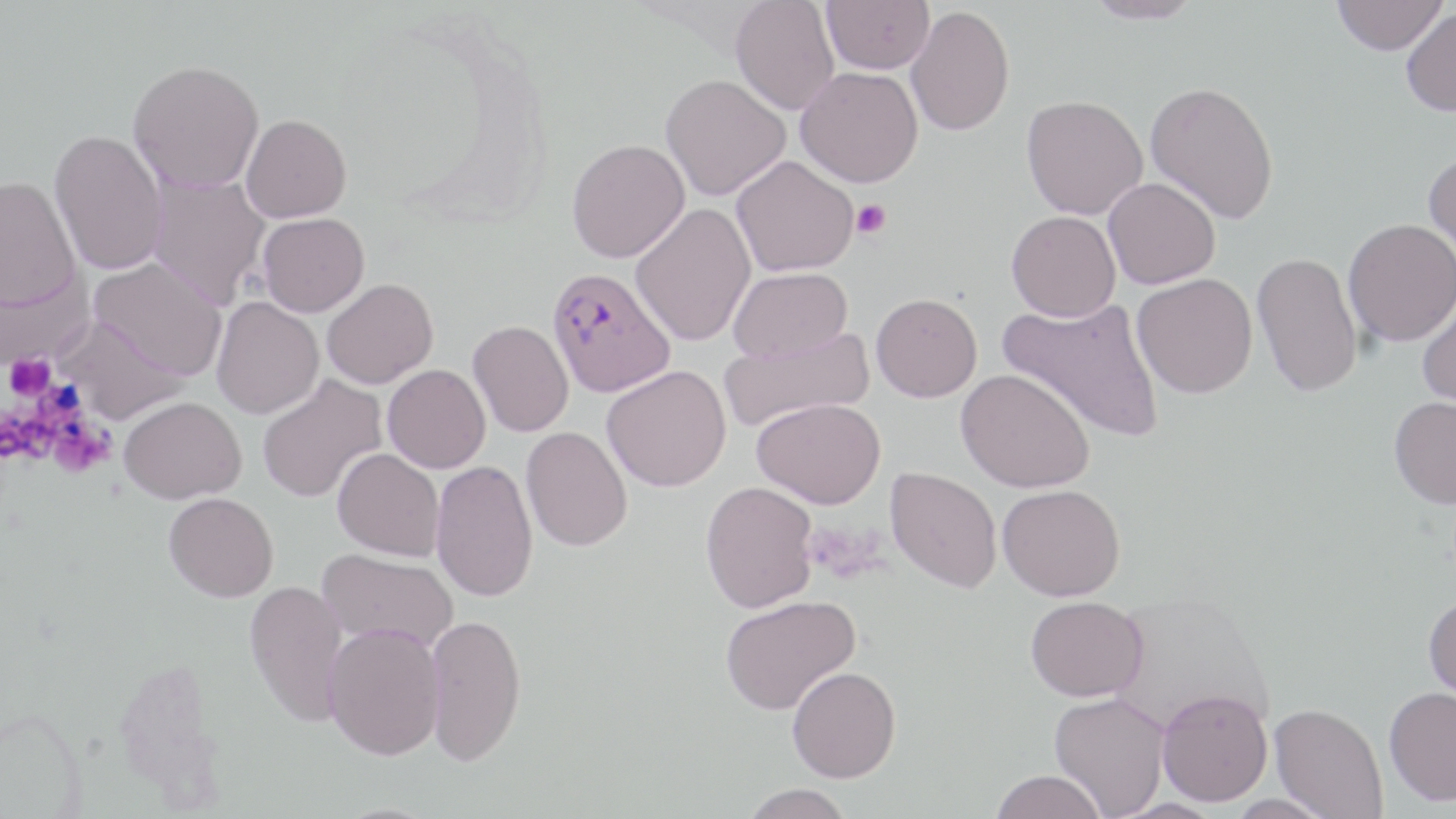

Summary:
  - Coordinate format: approximate bounding boxes as [x1, y1, x2, y2] in pixels
  - Plasmodium falciparum-infected red blood cell locations: [546, 267, 676, 398]
  - Uninfected red blood cell locations: [731, 0, 840, 115], [822, 0, 934, 74], [1083, 0, 1204, 24], [1331, 0, 1448, 55], [906, 6, 1015, 136], [1400, 7, 1456, 116], [128, 59, 264, 193], [795, 66, 923, 187], [661, 74, 790, 201], [1145, 81, 1279, 224], [1021, 95, 1148, 219], [241, 114, 352, 223], [49, 128, 169, 276], [566, 138, 690, 263], [1423, 149, 1456, 273], [732, 155, 859, 277], [147, 173, 272, 308], [0, 175, 80, 310], [1103, 177, 1220, 289], [630, 202, 756, 347], [1006, 210, 1121, 322], [258, 212, 369, 316], [1343, 219, 1456, 347], [1253, 252, 1363, 397], [89, 257, 227, 380], [729, 267, 853, 363], [0, 269, 93, 371], [1132, 274, 1257, 398], [322, 278, 438, 389], [871, 292, 982, 402], [1416, 293, 1456, 413], [998, 295, 1166, 443], [211, 297, 325, 418], [54, 314, 188, 424], [468, 320, 574, 437], [719, 328, 873, 433], [383, 364, 491, 473], [602, 365, 731, 492], [956, 369, 1094, 493], [257, 375, 388, 503], [1389, 395, 1456, 509], [119, 396, 246, 503], [752, 397, 885, 509], [521, 426, 633, 551], [332, 448, 446, 560], [430, 459, 539, 602], [886, 467, 1002, 593], [700, 481, 818, 613], [998, 484, 1126, 601], [164, 492, 278, 602], [318, 548, 459, 652], [244, 579, 349, 727], [1423, 593, 1456, 705], [719, 595, 861, 715], [1026, 595, 1148, 702], [425, 612, 526, 766], [323, 623, 445, 760], [786, 666, 901, 782], [1384, 686, 1456, 806], [1157, 688, 1273, 806], [1049, 692, 1171, 818], [1270, 703, 1389, 818], [991, 769, 1108, 819], [741, 783, 855, 819], [1223, 794, 1339, 818], [1110, 799, 1228, 819]
  - Platelet locations: [851, 199, 891, 239], [5, 354, 54, 400], [39, 385, 91, 429], [3, 409, 55, 468], [49, 423, 112, 476]
  - Slide-level diagnosis: Plasmodium falciparum
  - Modality: optical microscopy
  - Preparation: thin blood film
  - Magnification: 1000x
  - Field of view: single
  - Image size: 1456×819 pixels
  - Stain: May-Grünwald-Giemsa